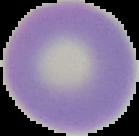

Result: no Plasmodium parasites seen. From a thin blood film. The area outside the segmented cell region is set to black. Image is 139×136 pixels.